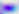
Summary:
  - Magnification: 400x
  - Modality: micrograph
  - Identification: Toxoplasma gondii